Comment on the morphology of the red blood cells.
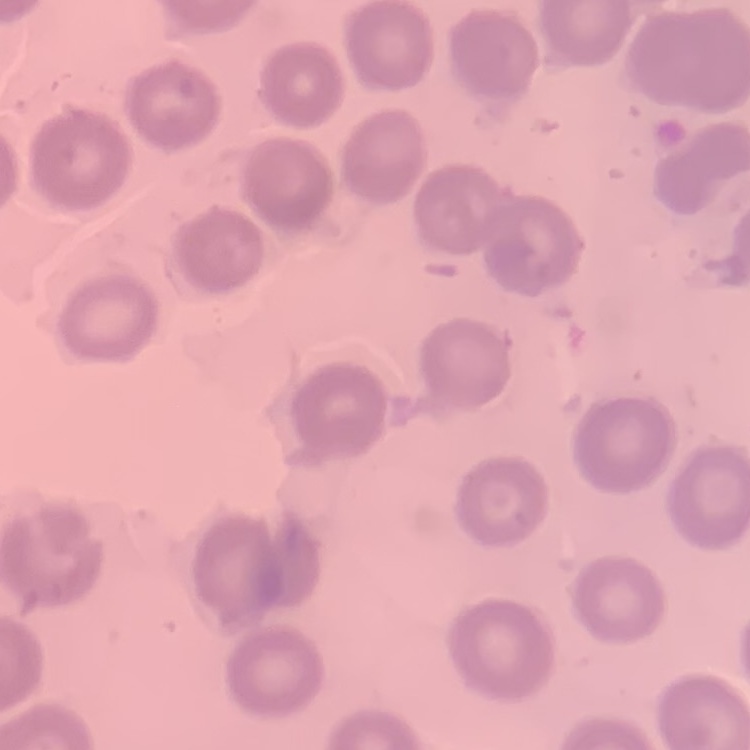

They show no rouleaux formation.

preparation = thin blood smear
stain = Field's or Giemsa
image type = square crop of a larger photomicrograph